Outline each blood parasite and name the species.
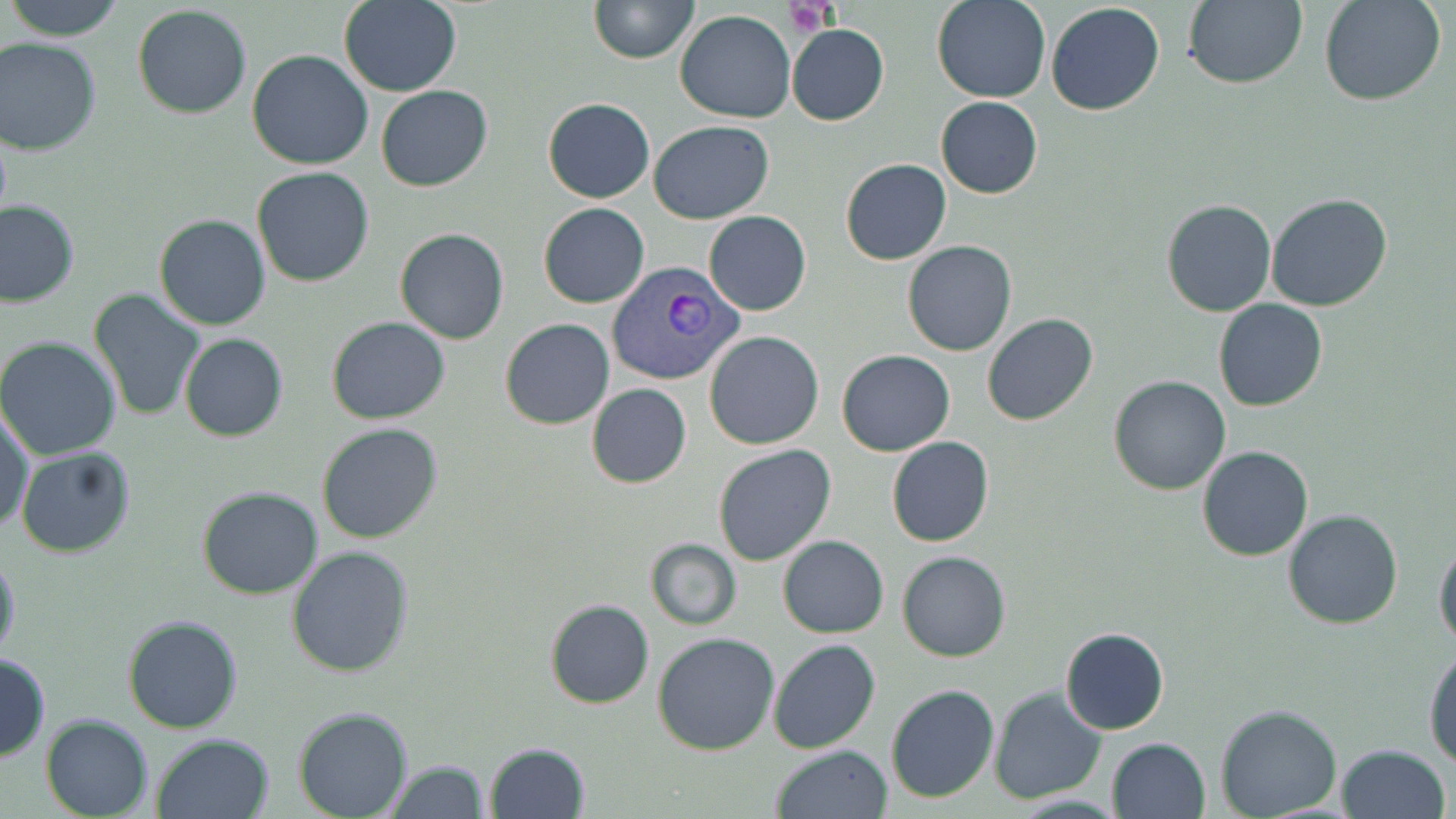

Approximate bounding boxes as named x1/y1/x2/y2 corners in pixels.
Plasmodium vivax-infected red blood cells: (x1=607, y1=263, x2=744, y2=387).
No Plasmodium falciparum, Plasmodium ovale, Plasmodium malariae, Babesia divergens, or Trypanosoma brucei observed.

Summary:
  - Platelet locations: (x1=783, y1=2, x2=839, y2=36)
  - Uninfected red blood cell locations: (x1=4, y1=0, x2=127, y2=41), (x1=339, y1=0, x2=462, y2=97), (x1=933, y1=0, x2=1051, y2=103), (x1=1182, y1=0, x2=1307, y2=89), (x1=1320, y1=0, x2=1446, y2=106), (x1=588, y1=1, x2=698, y2=64), (x1=1046, y1=3, x2=1165, y2=115), (x1=132, y1=5, x2=252, y2=118), (x1=675, y1=11, x2=796, y2=122), (x1=787, y1=24, x2=890, y2=126), (x1=0, y1=36, x2=102, y2=156), (x1=247, y1=49, x2=375, y2=170), (x1=376, y1=85, x2=493, y2=192), (x1=936, y1=96, x2=1042, y2=199), (x1=543, y1=99, x2=654, y2=203), (x1=0, y1=119, x2=12, y2=235), (x1=650, y1=120, x2=774, y2=225), (x1=840, y1=158, x2=951, y2=265), (x1=251, y1=165, x2=375, y2=287), (x1=1266, y1=193, x2=1394, y2=313), (x1=1160, y1=199, x2=1278, y2=318), (x1=0, y1=200, x2=80, y2=306), (x1=539, y1=203, x2=650, y2=308), (x1=703, y1=211, x2=812, y2=316), (x1=154, y1=213, x2=271, y2=330), (x1=394, y1=228, x2=509, y2=345), (x1=902, y1=240, x2=1017, y2=356), (x1=88, y1=289, x2=205, y2=421), (x1=1212, y1=299, x2=1328, y2=412), (x1=981, y1=313, x2=1098, y2=427), (x1=326, y1=317, x2=450, y2=423), (x1=499, y1=319, x2=615, y2=430), (x1=704, y1=330, x2=824, y2=450), (x1=179, y1=333, x2=289, y2=442), (x1=0, y1=337, x2=122, y2=461), (x1=836, y1=350, x2=956, y2=457), (x1=1108, y1=375, x2=1231, y2=495), (x1=586, y1=384, x2=693, y2=488), (x1=1, y1=405, x2=34, y2=535), (x1=316, y1=422, x2=444, y2=543), (x1=887, y1=436, x2=994, y2=547), (x1=713, y1=445, x2=836, y2=566), (x1=15, y1=446, x2=136, y2=558), (x1=1197, y1=446, x2=1314, y2=562), (x1=197, y1=487, x2=323, y2=599), (x1=1282, y1=510, x2=1403, y2=628), (x1=778, y1=536, x2=889, y2=638), (x1=645, y1=538, x2=742, y2=630), (x1=1434, y1=538, x2=1455, y2=650), (x1=287, y1=546, x2=415, y2=679), (x1=0, y1=549, x2=21, y2=666), (x1=897, y1=552, x2=1011, y2=661), (x1=543, y1=599, x2=655, y2=709), (x1=123, y1=614, x2=242, y2=734), (x1=1059, y1=626, x2=1169, y2=735), (x1=652, y1=632, x2=780, y2=755), (x1=769, y1=639, x2=881, y2=755), (x1=1424, y1=645, x2=1456, y2=768), (x1=0, y1=653, x2=49, y2=761), (x1=885, y1=684, x2=999, y2=802), (x1=990, y1=687, x2=1105, y2=803), (x1=1215, y1=704, x2=1343, y2=819), (x1=293, y1=707, x2=414, y2=819), (x1=39, y1=713, x2=154, y2=819), (x1=152, y1=734, x2=275, y2=819), (x1=1105, y1=737, x2=1213, y2=819), (x1=484, y1=741, x2=591, y2=818), (x1=1335, y1=743, x2=1450, y2=819), (x1=771, y1=744, x2=894, y2=819), (x1=384, y1=759, x2=491, y2=819)
  - Slide-level diagnosis: Plasmodium vivax
  - Field of view: one of a larger specimen
  - Stain: May-Grünwald-Giemsa
  - Magnification: 1000x
  - Image size: 1456×819 pixels
  - Modality: optical microscopy
  - Preparation: thin blood film